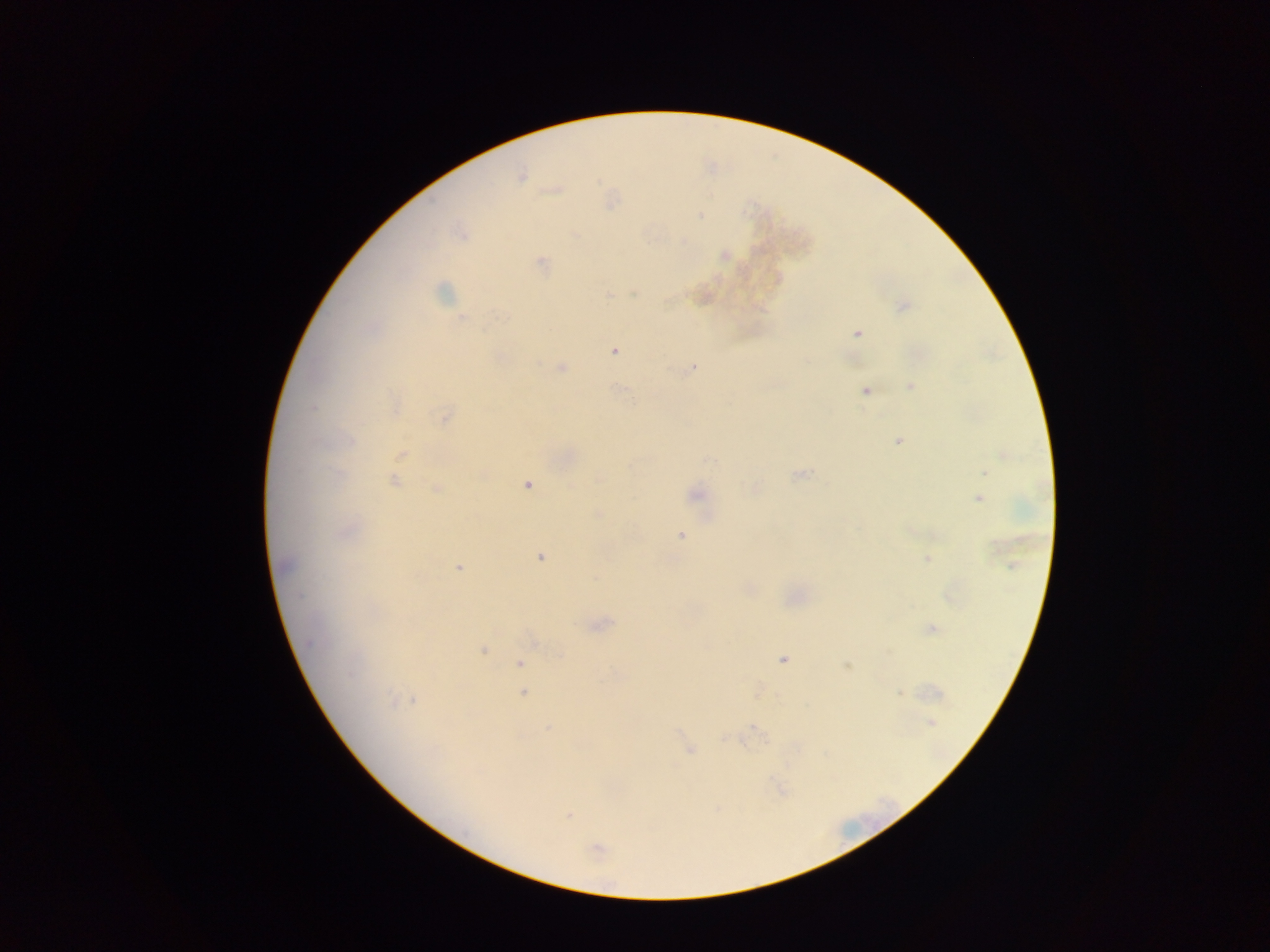
{
  "capture": "mobile-phone photograph through a microscope",
  "preparation": "thick blood smear",
  "malaria_parasite_locations": "approximate centers as (x, y) in pixels: (520, 174), (700, 216), (725, 254), (541, 262), (608, 294), (902, 307), (461, 319), (858, 334), (614, 351), (500, 358), (561, 367), (693, 367), (910, 386), (865, 391), (314, 407), (444, 418), (350, 440), (898, 441), (402, 454), (709, 461), (982, 473), (799, 476), (394, 480), (527, 485), (437, 488), (755, 489), (695, 494), (978, 498), (597, 514), (681, 535), (540, 557), (927, 558), (458, 567), (299, 595), (601, 625), (932, 628), (312, 642), (534, 643), (483, 651), (782, 660), (520, 664), (847, 666), (350, 675), (523, 693), (899, 693), (414, 701), (391, 702), (931, 722), (549, 728), (755, 729), (678, 732), (724, 738), (689, 750), (568, 815), (597, 849)",
  "field_of_view": "single",
  "image_size": "1270×952 pixels",
  "country": "Ghana"
}